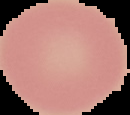

Summary:
  - Image type: segmented cell region with the area outside set to black
  - Result: no malaria parasites detected
  - Image size: 130×115 pixels
  - Preparation: thin blood film